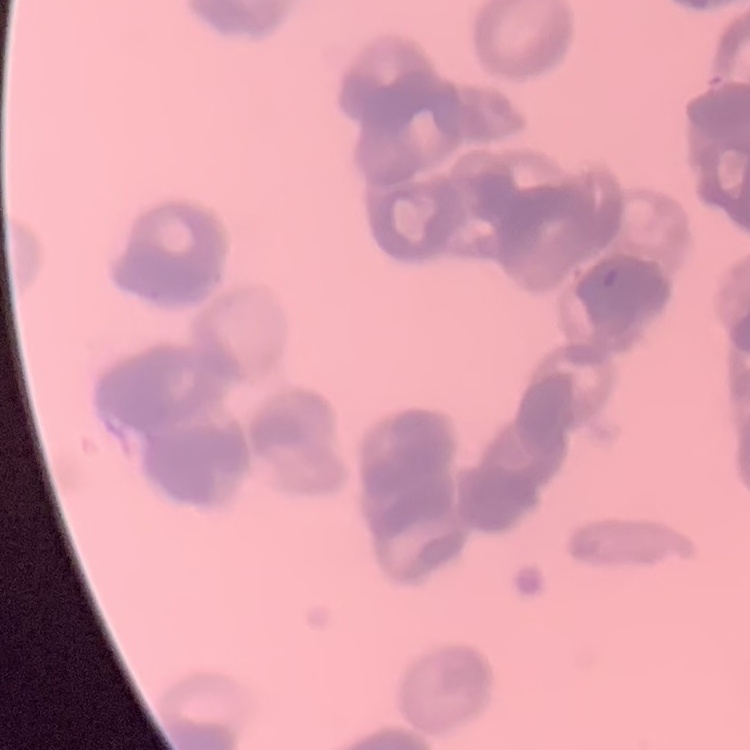

erythrocyte morphology = rouleaux formation
image type = one tile cut from a larger photomicrograph
preparation = thin peripheral smear
stain = Field's or Giemsa